State which parasite is depicted.
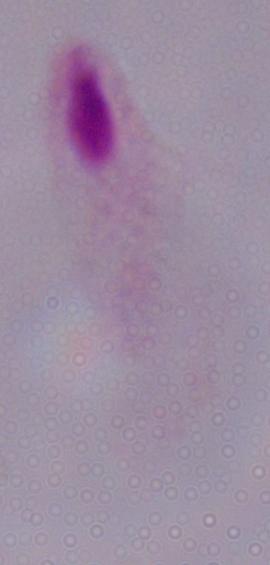

This is a trichomonad.

1000x magnification. Micrograph.